Locate every uninfected red blood cell.
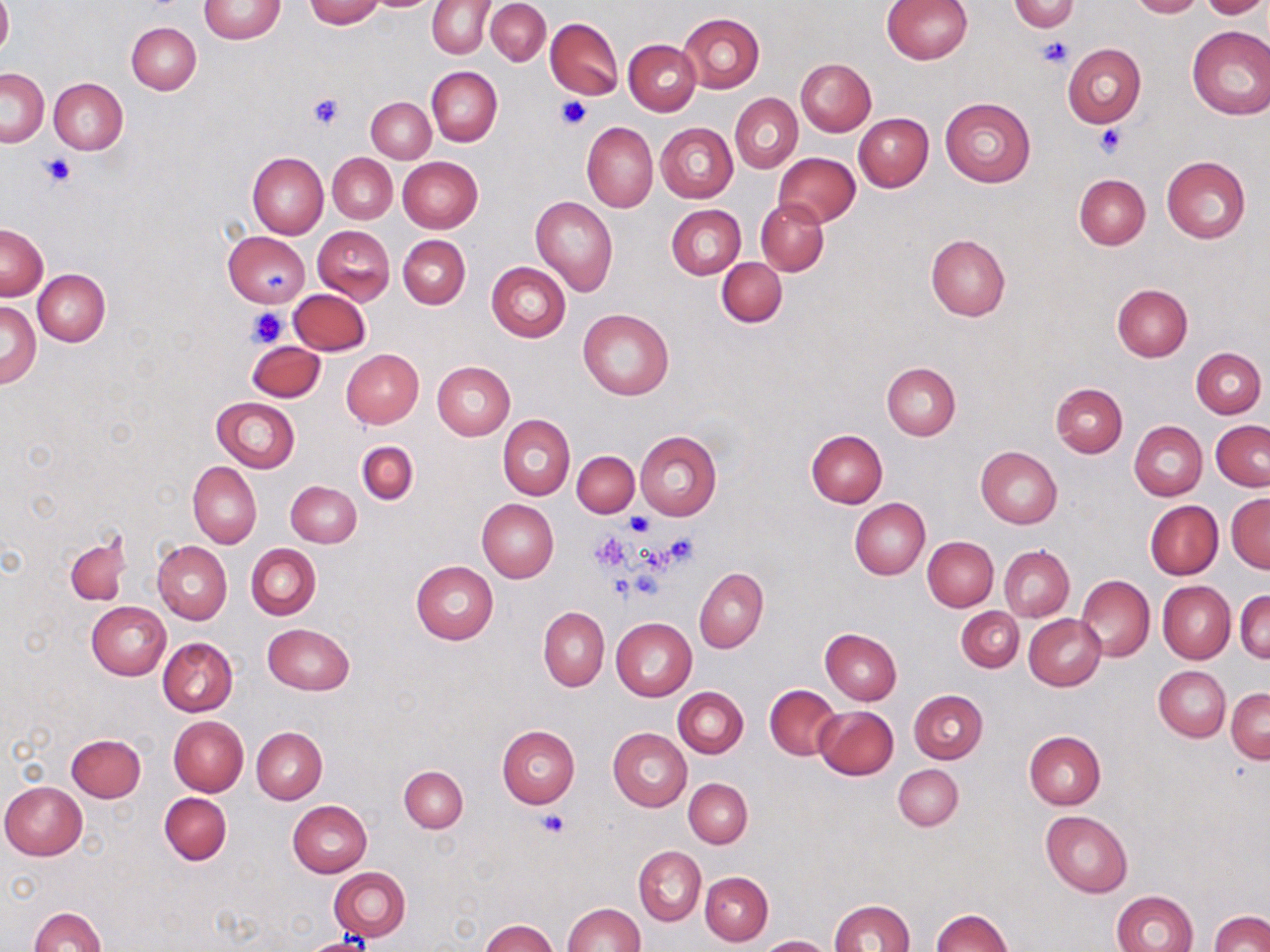

Approximate bounding boxes as (x1, y1, x2, y2) in pixels.
Uninfected red blood cells: (198, 0, 287, 43), (305, 0, 384, 27), (370, 0, 438, 10), (486, 0, 551, 65), (882, 0, 971, 64), (1127, 0, 1205, 18), (1200, 0, 1267, 20), (0, 1, 12, 59), (428, 1, 493, 59), (1010, 1, 1081, 32), (677, 13, 765, 93), (545, 19, 622, 99), (126, 22, 201, 95), (1187, 25, 1270, 120), (624, 39, 701, 115), (1062, 43, 1145, 127), (796, 58, 876, 136), (0, 67, 49, 146), (426, 67, 503, 146), (50, 78, 127, 154), (730, 92, 803, 174), (940, 96, 1036, 186), (366, 97, 435, 163), (853, 113, 933, 191), (583, 122, 658, 212), (656, 123, 737, 203), (248, 151, 328, 239), (327, 153, 396, 222), (774, 153, 861, 228), (1161, 156, 1251, 243), (398, 157, 483, 232), (1074, 174, 1150, 249), (531, 197, 618, 296), (756, 198, 828, 276), (666, 205, 745, 279), (0, 224, 47, 300), (313, 226, 394, 303), (224, 231, 310, 309), (926, 235, 1010, 321), (399, 236, 470, 309), (717, 257, 787, 327), (486, 263, 571, 343), (33, 269, 110, 346), (1112, 283, 1193, 361), (289, 289, 370, 355), (2, 301, 40, 388), (578, 307, 673, 400), (247, 341, 325, 402), (1191, 347, 1266, 418), (341, 349, 424, 428), (432, 362, 514, 440), (881, 363, 960, 440), (1051, 382, 1128, 457), (212, 397, 299, 472), (498, 416, 574, 499), (1130, 421, 1207, 501), (1210, 421, 1269, 491), (805, 429, 887, 508), (634, 431, 722, 519), (357, 441, 417, 504), (976, 446, 1063, 528), (572, 450, 639, 517), (189, 462, 261, 547), (286, 480, 360, 547), (1227, 494, 1270, 572), (848, 498, 929, 579), (477, 499, 558, 583), (1146, 500, 1222, 579), (65, 536, 131, 605), (923, 536, 998, 611), (153, 541, 232, 625), (246, 544, 320, 620), (999, 545, 1074, 621), (411, 560, 498, 644), (695, 567, 768, 652), (1076, 574, 1155, 662), (1158, 582, 1235, 664), (1235, 589, 1270, 664), (87, 601, 171, 680), (539, 607, 609, 690), (957, 607, 1023, 672), (1024, 614, 1106, 690), (612, 618, 697, 701), (262, 623, 355, 695), (821, 628, 902, 704), (158, 637, 237, 716), (1154, 665, 1230, 741), (765, 685, 841, 760), (673, 687, 748, 757), (1226, 688, 1269, 764), (908, 689, 988, 763), (814, 705, 898, 780), (169, 716, 249, 796), (496, 725, 579, 807), (252, 727, 327, 804), (608, 728, 691, 811), (1024, 731, 1105, 809), (66, 733, 146, 801), (893, 764, 963, 831), (399, 765, 468, 832), (684, 778, 752, 848), (0, 782, 86, 860), (160, 793, 231, 865), (287, 800, 372, 877), (1041, 810, 1133, 896), (633, 845, 706, 926), (329, 866, 411, 940), (700, 871, 772, 946), (1112, 890, 1197, 952), (829, 900, 915, 952), (562, 902, 644, 952), (29, 906, 104, 952), (931, 908, 1013, 952), (1209, 911, 1270, 952), (480, 919, 559, 952), (757, 935, 833, 952), (300, 936, 376, 952).

{
  "slide_level_diagnosis": "negative for blood parasites",
  "modality": "light microscopy",
  "stain": "May-Grünwald-Giemsa",
  "platelet_locations": "approximate bounding boxes as (x1, y1, x2, y2) in pixels: (1039, 36, 1072, 68), (307, 95, 344, 129), (555, 95, 592, 131), (1095, 123, 1126, 157), (42, 153, 76, 187), (264, 271, 289, 293), (247, 307, 288, 348), (625, 513, 653, 537), (590, 530, 632, 573), (655, 535, 698, 569), (632, 569, 662, 600), (609, 576, 633, 603), (537, 809, 570, 837)",
  "field_of_view": "single",
  "magnification": "1000x",
  "image_size": "1270×952 pixels",
  "preparation": "thin blood smear"
}